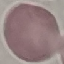 Result: negative for malaria parasites. Giemsa-stained preparation. Photographed with a smartphone camera at the microscope eyepiece. Automatically extracted cell patch, resized to 64 × 64 pixels. Thin blood film.